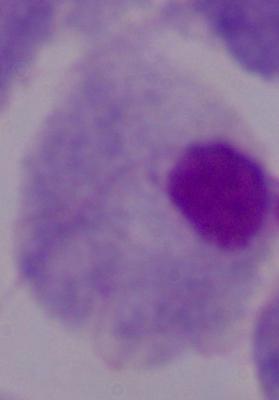

identification = trichomonad
magnification = 1000x
modality = micrograph